Identify the parasite.
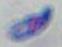

Toxoplasma gondii.

modality = photomicrograph
magnification = 1000x